Outline each Plasmodium ovale-infected red blood cell.
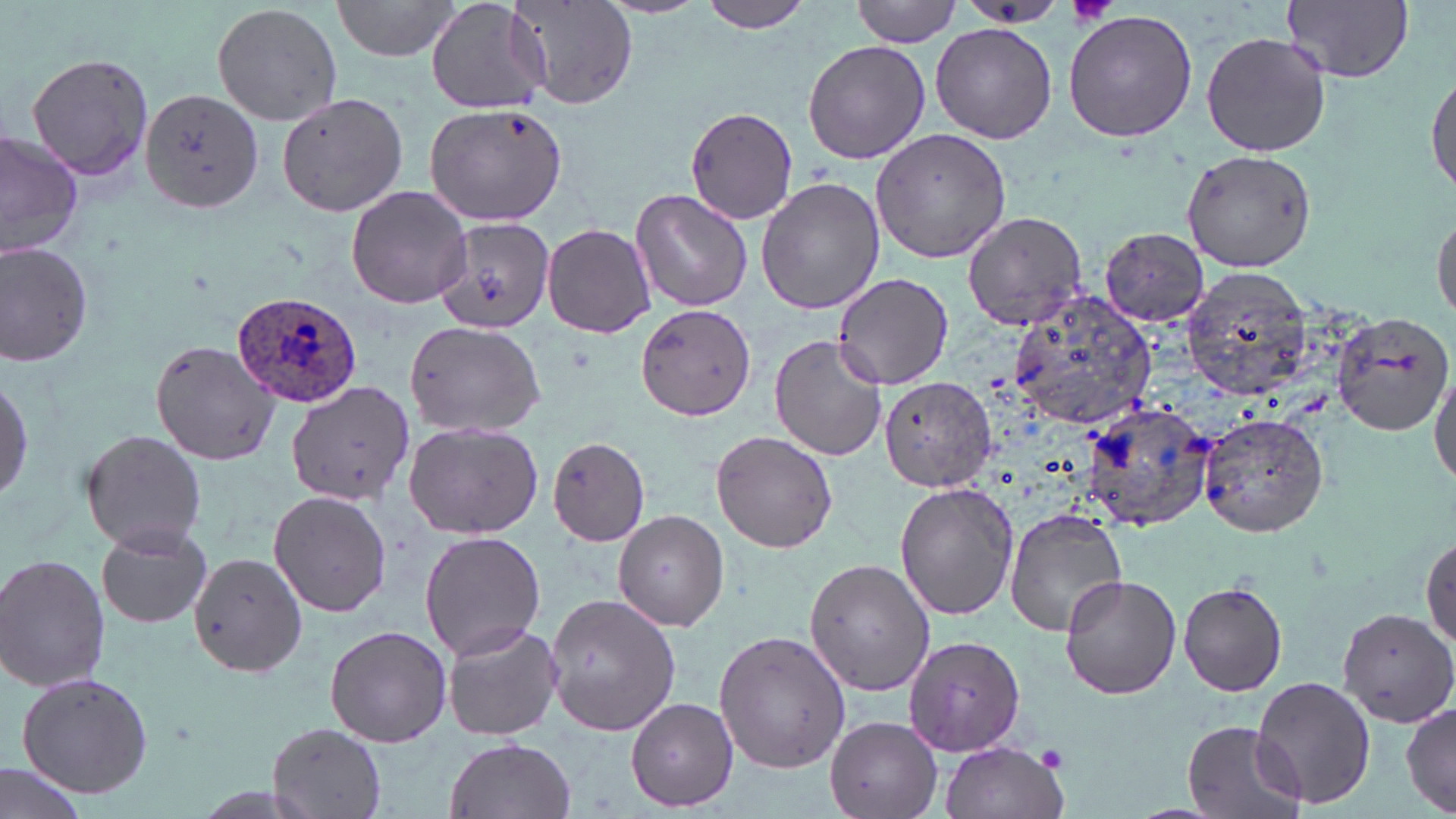

Approximate bounding boxes as (x1,y1)-(x2,y2) corner pairs in pixels.
Plasmodium ovale-infected red blood cells: (230,292)-(363,407).

slide-level diagnosis = Plasmodium ovale
image size = 1456×819 pixels
modality = optical microscopy
field of view = single
platelet locations = approximate bounding boxes as (x1,y1)-(x2,y2) corner pairs in pixels: (1067,0)-(1120,27), (1037,747)-(1068,772)
preparation = thin blood smear
uninfected red blood cell locations = approximate bounding boxes as (x1,y1)-(x2,y2) corner pairs in pixels: (330,0)-(468,63), (424,0)-(552,115), (513,0)-(637,110), (696,0)-(817,34), (853,0)-(962,47), (1284,0)-(1413,83), (956,1)-(1070,26), (212,2)-(344,127), (1063,11)-(1198,142), (930,22)-(1057,143), (1201,29)-(1332,157), (802,39)-(931,165), (27,53)-(153,183), (1428,63)-(1456,197), (141,87)-(263,212), (276,91)-(408,216), (424,101)-(567,226), (684,105)-(799,224), (869,129)-(1010,265), (0,130)-(80,259), (1182,150)-(1320,272), (756,175)-(884,317), (346,185)-(473,310), (630,188)-(753,313), (1433,208)-(1455,328), (961,209)-(1089,331), (434,218)-(557,334), (542,222)-(658,339), (1098,228)-(1209,326), (0,241)-(95,368), (1181,266)-(1313,398), (832,272)-(956,389), (1001,291)-(1161,430), (636,304)-(757,422), (1334,311)-(1455,434), (404,320)-(546,439), (770,334)-(887,462), (148,337)-(278,467), (1431,367)-(1456,488), (0,373)-(32,504), (880,374)-(997,493), (285,379)-(413,506), (1076,392)-(1215,534), (1199,410)-(1328,537), (404,422)-(544,538), (80,430)-(208,551), (710,431)-(839,553), (546,436)-(651,546), (895,481)-(1020,621), (269,491)-(391,618), (1003,508)-(1129,639), (614,510)-(729,631), (95,523)-(214,629), (419,530)-(546,658), (1421,532)-(1455,658), (187,551)-(308,678), (0,553)-(110,691), (803,558)-(936,696), (1059,573)-(1182,700), (1179,579)-(1288,697), (543,592)-(680,738), (1339,604)-(1456,726), (441,620)-(563,741), (325,623)-(452,748), (715,630)-(850,774), (902,633)-(1027,758), (16,671)-(154,798), (1250,675)-(1376,810), (626,696)-(738,811), (1400,700)-(1456,815), (828,717)-(941,818), (1180,720)-(1308,819), (267,723)-(389,817), (445,738)-(575,819), (939,740)-(1067,819), (0,760)-(90,819)
magnification = 1000x
stain = May-Grünwald-Giemsa